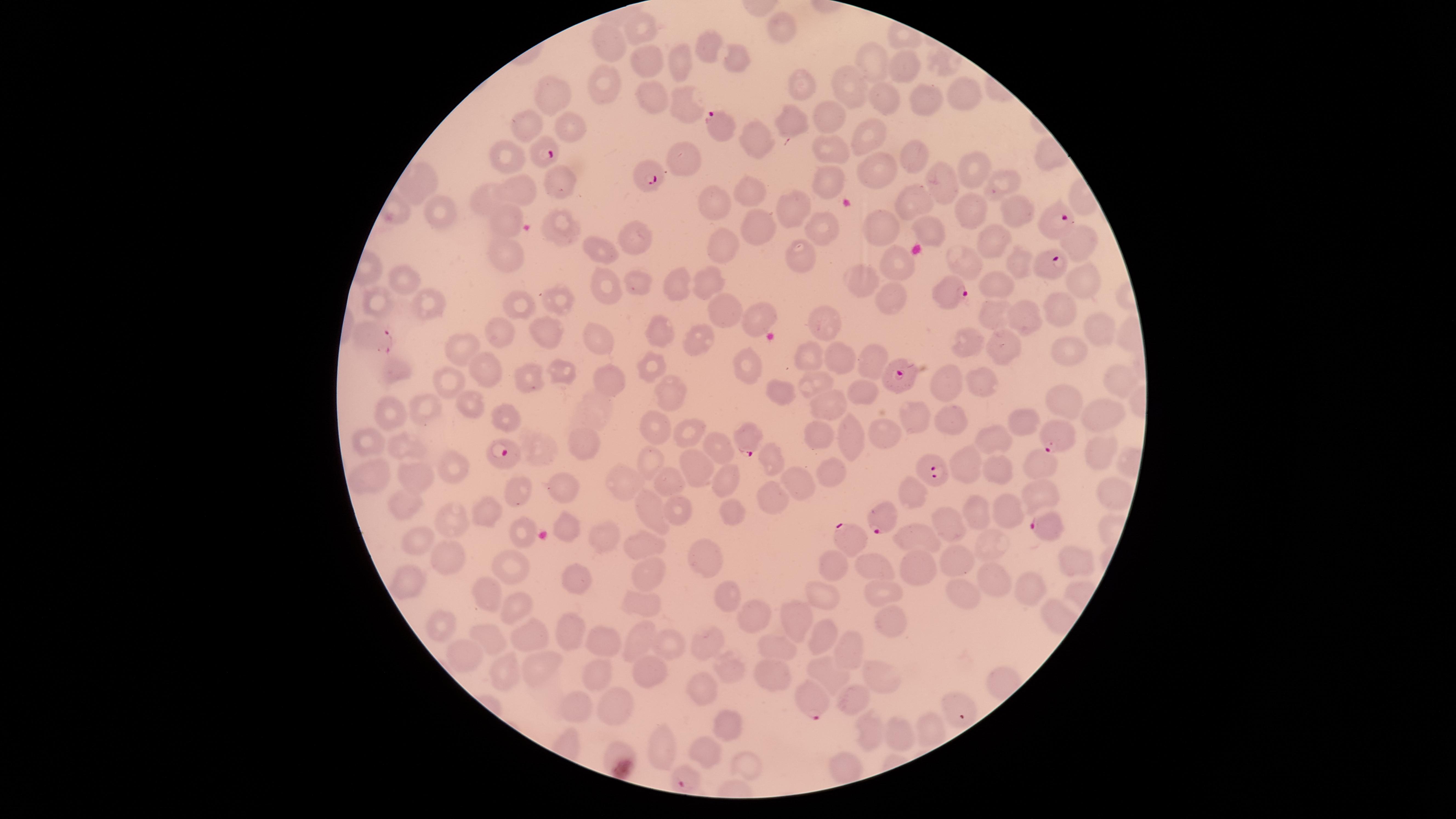

Approximate marker points as {x, y} in pixels.
Summary:
  - Parasitized red blood cells: {726, 126}, {545, 153}, {652, 169}, {1051, 222}, {1047, 264}, {951, 295}, {368, 333}, {900, 375}, {1060, 437}, {749, 438}, {504, 459}, {928, 469}, {881, 522}, {1042, 526}, {851, 540}, {814, 702}, {956, 709}, {685, 780}
  - Uninfected red blood cells: {646, 29}, {779, 29}, {605, 41}, {707, 46}, {738, 59}, {681, 63}, {647, 64}, {905, 66}, {871, 68}, {604, 79}, {849, 85}, {798, 87}, {965, 93}, {555, 95}, {880, 98}, {925, 102}, {684, 104}, {655, 105}, {825, 117}, {787, 121}, {526, 124}, {570, 126}, {864, 137}, {758, 140}, {913, 154}, {509, 155}, {691, 156}, {827, 159}, {973, 169}, {879, 173}, {939, 173}, {826, 176}, {1003, 178}, {558, 180}, {419, 182}, {526, 191}, {750, 191}, {492, 194}, {715, 206}, {789, 206}, {910, 206}, {1022, 213}, {437, 214}, {970, 214}, {510, 220}, {763, 223}, {563, 224}, {884, 227}, {826, 230}, {928, 234}, {644, 239}, {995, 241}, {1082, 242}, {601, 249}, {725, 249}, {515, 254}, {805, 256}, {968, 261}, {893, 262}, {1017, 266}, {410, 278}, {640, 281}, {678, 282}, {1081, 284}, {856, 285}, {999, 286}, {709, 288}, {609, 291}, {887, 295}, {379, 298}, {561, 299}, {431, 302}, {518, 305}, {1058, 309}, {730, 313}, {756, 316}, {993, 316}, {1024, 318}, {824, 321}, {1097, 329}, {662, 331}, {590, 335}, {508, 339}, {550, 339}, {701, 341}, {968, 347}, {1006, 352}, {464, 353}, {1065, 354}, {747, 360}, {840, 361}, {807, 362}, {650, 364}, {871, 366}, {486, 369}, {556, 370}, {398, 372}, {529, 377}, {608, 379}, {1119, 379}, {942, 382}, {451, 384}, {983, 385}, {810, 387}, {866, 389}, {669, 391}, {780, 394}, {837, 402}, {1068, 403}, {470, 406}, {423, 409}, {390, 410}, {1098, 412}, {921, 414}, {508, 419}, {957, 419}, {1031, 425}, {656, 427}, {888, 433}, {689, 435}, {369, 436}, {586, 440}, {858, 440}, {819, 441}, {999, 442}, {400, 446}, {714, 448}, {1103, 451}, {545, 453}, {647, 458}, {772, 458}, {967, 467}, {830, 469}, {700, 471}, {992, 471}, {1042, 472}, {456, 475}, {373, 477}, {409, 477}, {616, 477}, {664, 479}, {721, 480}, {797, 481}, {559, 489}, {907, 493}, {1038, 493}, {522, 494}, {1110, 494}, {773, 496}, {404, 503}, {647, 505}, {1008, 505}, {679, 509}, {730, 510}, {978, 510}, {486, 512}, {453, 516}, {951, 519}, {568, 525}, {520, 531}, {605, 531}, {915, 538}, {421, 542}, {994, 544}, {637, 546}, {956, 556}, {1068, 558}, {701, 559}, {450, 561}, {834, 566}, {875, 566}, {919, 567}, {510, 571}, {643, 575}, {582, 580}, {406, 582}, {998, 584}, {957, 589}, {872, 591}, {1032, 591}, {484, 592}, {726, 595}, {828, 597}, {639, 603}, {517, 608}, {751, 614}, {795, 615}, {885, 620}, {444, 629}, {571, 631}, {641, 637}, {819, 637}, {490, 638}, {525, 638}, {602, 638}, {708, 644}, {672, 645}, {846, 646}, {779, 647}, {472, 658}, {539, 668}, {596, 668}, {728, 669}, {500, 670}, {832, 671}, {645, 672}, {881, 673}, {772, 676}, {702, 690}, {856, 701}, {619, 704}, {579, 705}, {732, 726}, {932, 728}, {870, 733}, {901, 734}, {668, 744}, {615, 750}, {706, 753}, {744, 764}, {845, 765}
  - Field of view: single
  - Preparation: thin blood film
  - Visible region: circular
  - Stain: Giemsa
  - Capture: smartphone photograph through the microscope eyepiece
  - Presence: malaria parasites identified
  - Image size: 1456×819 pixels
  - Species: Plasmodium falciparum